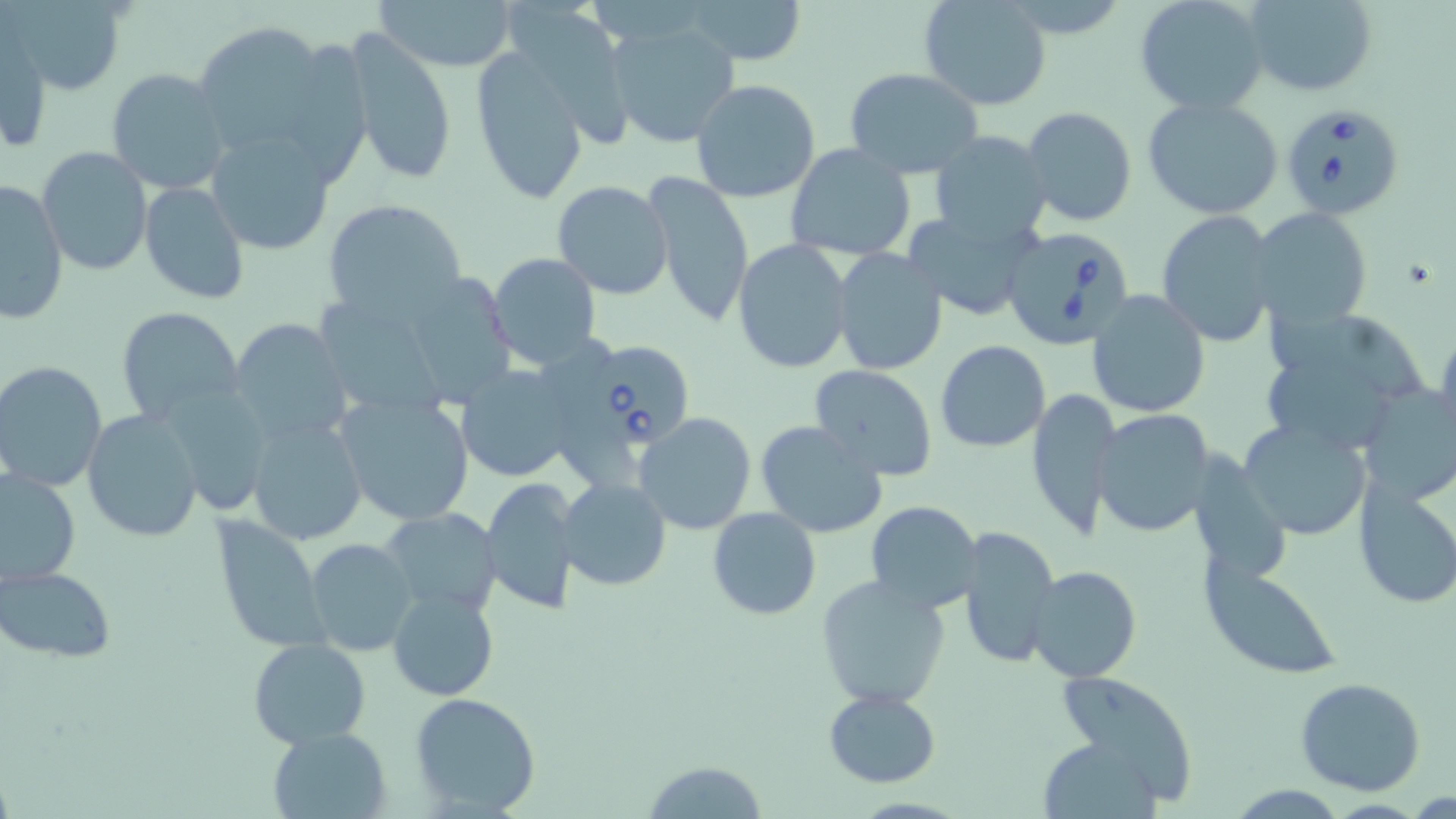
Approximate bounding boxes as (x1,y1)-(x2,y2) corner pairs in pixels. Uninfected red blood cell locations: (3,0)-(128,94), (376,0)-(518,73), (680,0)-(810,66), (919,0)-(1053,112), (1133,0)-(1272,116), (1241,0)-(1378,96), (609,17)-(742,150), (192,18)-(353,168), (1,30)-(51,155), (342,31)-(457,188), (469,46)-(594,204), (106,68)-(232,195), (844,68)-(987,179), (691,79)-(822,203), (1141,95)-(1284,219), (1023,106)-(1137,227), (206,128)-(337,257), (931,130)-(1055,247), (785,142)-(916,264), (38,147)-(153,277), (642,170)-(754,330), (1,179)-(69,323), (551,180)-(675,300), (139,181)-(249,303), (321,196)-(469,325), (1250,208)-(1372,332), (902,209)-(1041,320), (1155,211)-(1279,345), (732,238)-(853,374), (832,248)-(948,376), (486,253)-(601,372), (392,268)-(519,408), (1086,292)-(1210,418), (321,300)-(443,419), (1257,303)-(1431,455), (115,307)-(246,427), (228,318)-(355,447), (1434,319)-(1456,443), (936,341)-(1051,452), (0,360)-(106,492), (455,362)-(576,485), (808,364)-(939,482), (1355,380)-(1456,506), (1026,386)-(1121,541), (163,388)-(272,515), (334,388)-(477,528), (82,409)-(203,544), (1092,410)-(1218,538), (633,412)-(758,535), (245,413)-(368,546), (1238,417)-(1373,540), (754,420)-(889,538), (1,468)-(80,587), (1352,474)-(1456,610), (483,475)-(581,614), (559,478)-(671,590), (864,501)-(984,613), (379,507)-(503,619), (708,508)-(820,620), (209,516)-(331,653), (956,524)-(1060,667), (303,539)-(419,657), (1200,557)-(1345,679), (1026,564)-(1142,682), (0,565)-(115,663), (816,575)-(950,709), (387,586)-(497,700), (248,638)-(372,749), (1058,671)-(1201,802), (1295,676)-(1427,796), (825,689)-(941,786), (409,691)-(542,816), (268,726)-(392,818), (1039,736)-(1163,818), (643,760)-(768,818), (1225,784)-(1349,816). Babesia divergens-infected red blood cell locations: (1279,104)-(1407,220), (1003,227)-(1137,351), (574,333)-(700,460). Slide-level diagnosis: Babesia divergens. Thin blood smear. Single field of view. Image is 1456×819 pixels. Light microscopy. May-Grünwald-Giemsa stain. Captured at 1000x magnification.